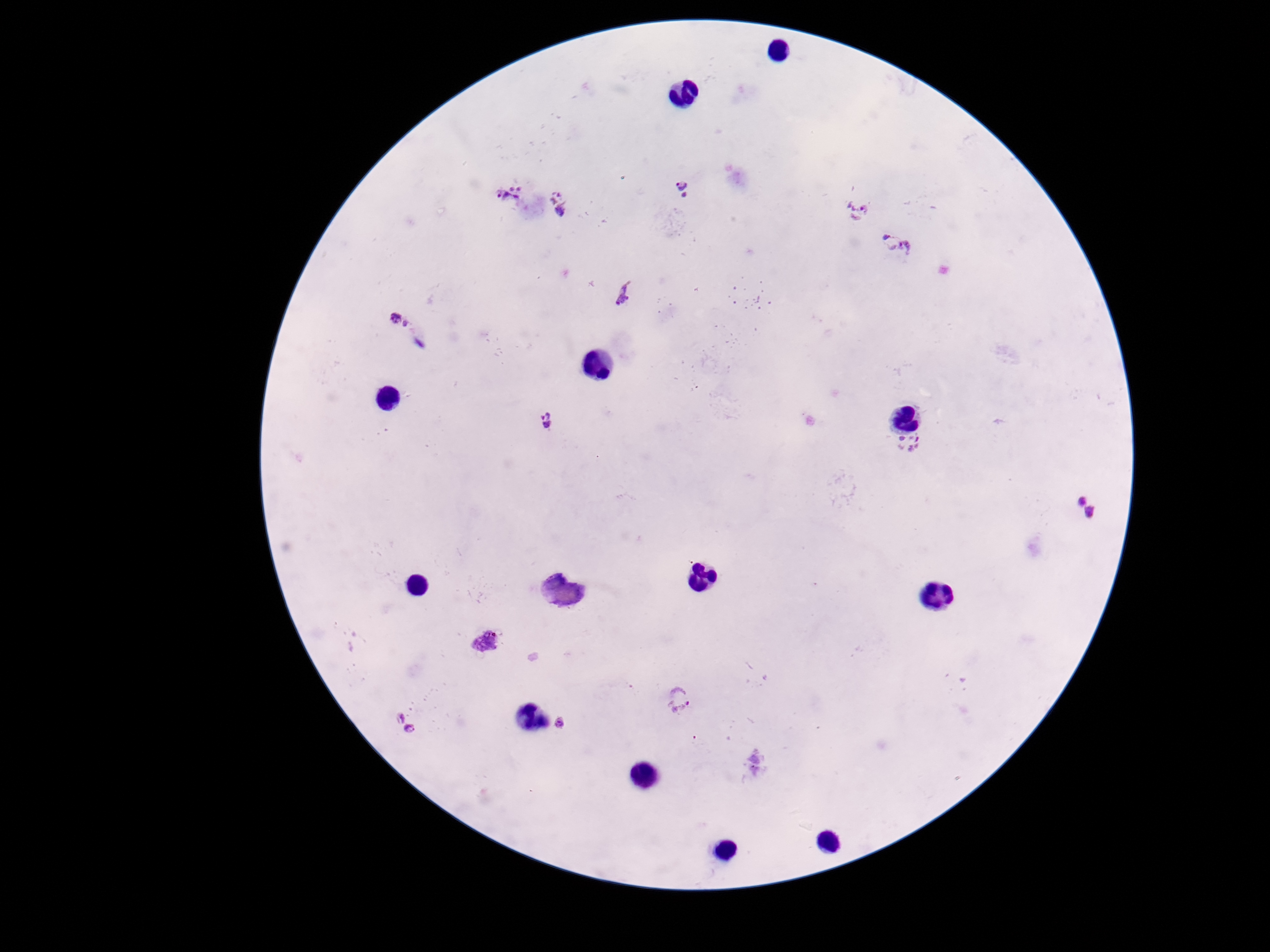 Approximate centers as {x, y} in pixels. Plasmodium parasite locations: {683, 187}, {508, 193}, {559, 203}, {858, 212}, {898, 244}, {622, 295}, {399, 320}, {545, 419}, {908, 444}, {1084, 507}, {486, 643}, {680, 699}, {560, 723}, {405, 724}. Giemsa-stained preparation. Patient malaria status: positive. Image is 1270×952 pixels. Photographed through the microscope eyepiece with a smartphone camera. Thick blood film. 100x magnification. One field from this slide.